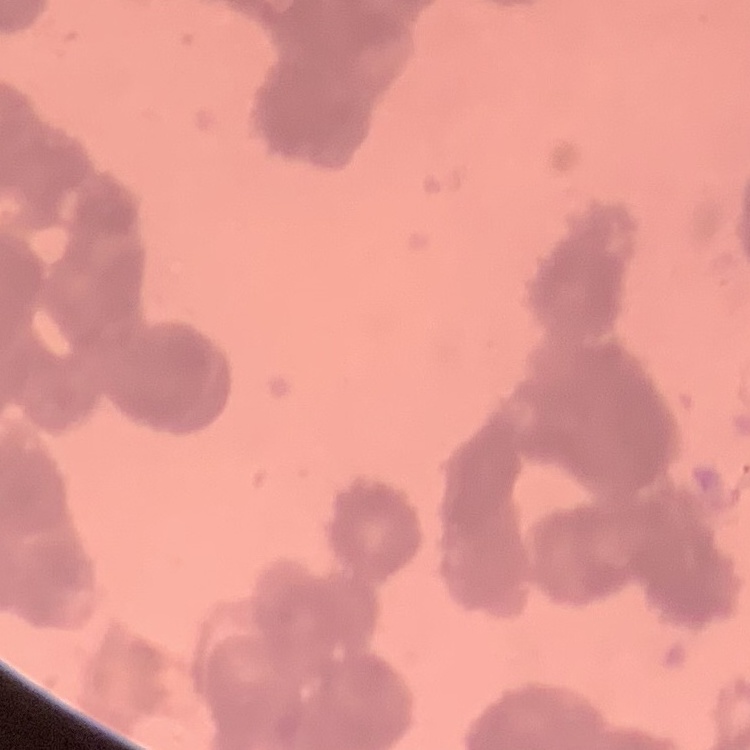

The erythrocytes exhibit rouleaux formation. Square crop of a larger photomicrograph. Stained with either Field's or Giemsa. Thin peripheral smear.